Identify the blood parasite species.
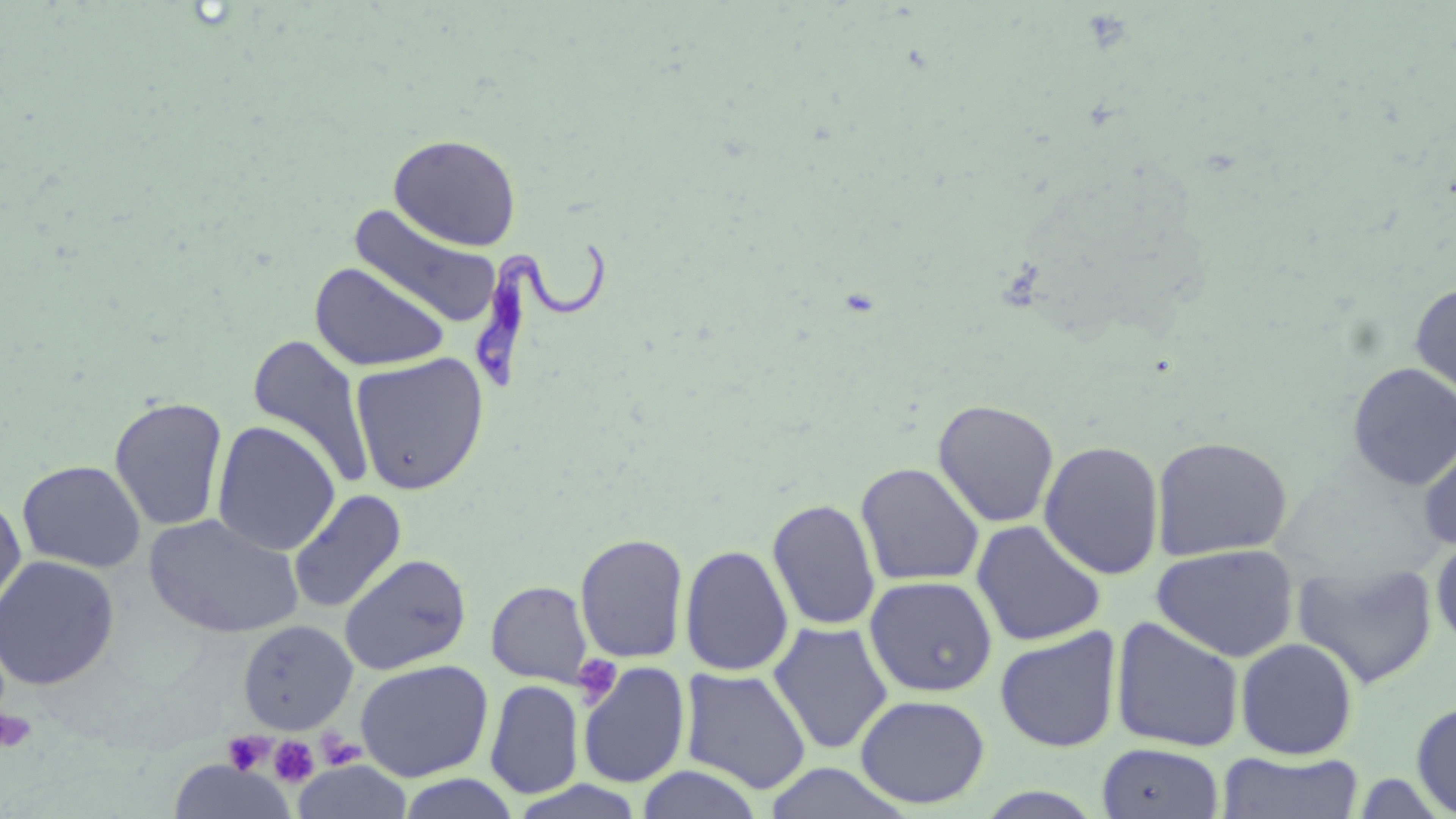
Trypanosoma brucei.

Approximate bounding boxes as [x1, y1, x2, y2] in pixels. Platelet locations: [573, 654, 622, 707], [0, 710, 37, 752], [317, 729, 364, 769], [222, 732, 273, 774], [269, 736, 319, 788]. Trypanosoma brucei locations: [471, 238, 611, 398]. Uninfected red blood cell locations: [388, 133, 522, 251], [348, 205, 504, 331], [309, 263, 449, 371], [1410, 281, 1456, 406], [247, 334, 376, 492], [350, 352, 490, 495], [1347, 362, 1456, 489], [109, 395, 229, 532], [932, 399, 1060, 528], [212, 421, 341, 556], [1416, 430, 1456, 554], [1151, 435, 1293, 561], [1039, 439, 1166, 579], [17, 459, 145, 573], [855, 461, 985, 586], [288, 489, 407, 613], [0, 493, 27, 619], [767, 498, 881, 632], [145, 512, 305, 640], [971, 519, 1107, 646], [574, 532, 690, 663], [1430, 535, 1456, 654], [1152, 543, 1300, 662], [680, 544, 794, 676], [339, 553, 472, 675], [0, 555, 120, 690], [1292, 560, 1438, 689], [864, 575, 997, 697], [486, 580, 594, 687], [1109, 616, 1245, 752], [237, 620, 357, 735], [768, 621, 894, 754], [995, 627, 1122, 752], [1235, 637, 1359, 759], [355, 659, 493, 782], [577, 661, 691, 788], [679, 667, 812, 794], [486, 679, 583, 799], [855, 693, 990, 809], [1411, 699, 1456, 816], [1096, 742, 1225, 818], [1219, 751, 1365, 818], [168, 760, 294, 819], [292, 760, 414, 819], [762, 764, 909, 817], [635, 766, 765, 819], [395, 773, 519, 818]. One field of a larger specimen. Thin blood film. Light microscopy. Captured at 1000x magnification. Image is 1456×819 pixels. May-Grünwald-Giemsa-stained preparation.